Identify the cell.
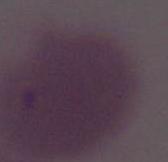
An erythrocyte.

Summary:
  - Modality: micrograph
  - Magnification: 1000x